State the blood parasite species.
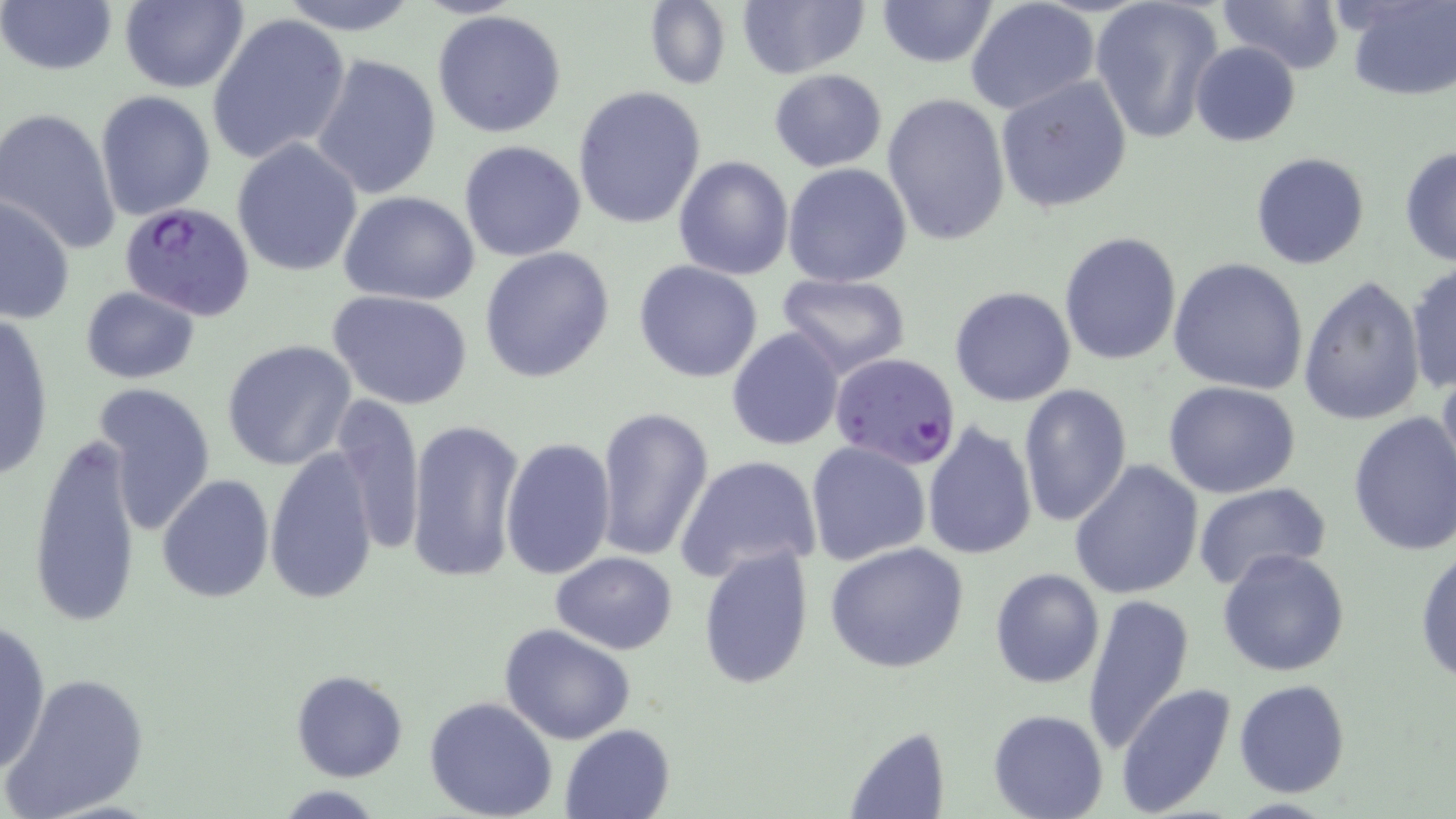

Plasmodium falciparum.

Approximate bounding boxes as named x1/y1/x2/y2 corners in pixels. Plasmodium falciparum-infected red blood cell locations: (x1=118, y1=199, x2=257, y2=323), (x1=830, y1=351, x2=961, y2=468). Uninfected red blood cell locations: (x1=118, y1=0, x2=249, y2=94), (x1=273, y1=0, x2=422, y2=34), (x1=735, y1=0, x2=869, y2=78), (x1=1089, y1=0, x2=1224, y2=144), (x1=1218, y1=0, x2=1346, y2=75), (x1=1341, y1=0, x2=1456, y2=100), (x1=2, y1=1, x2=119, y2=78), (x1=876, y1=1, x2=997, y2=70), (x1=642, y1=2, x2=732, y2=90), (x1=965, y1=2, x2=1099, y2=117), (x1=432, y1=9, x2=568, y2=137), (x1=208, y1=13, x2=352, y2=167), (x1=1190, y1=42, x2=1301, y2=147), (x1=311, y1=54, x2=443, y2=200), (x1=769, y1=69, x2=887, y2=172), (x1=995, y1=75, x2=1134, y2=212), (x1=571, y1=85, x2=707, y2=230), (x1=94, y1=89, x2=217, y2=223), (x1=882, y1=91, x2=1012, y2=248), (x1=0, y1=105, x2=122, y2=257), (x1=231, y1=139, x2=363, y2=276), (x1=459, y1=139, x2=586, y2=261), (x1=1398, y1=144, x2=1456, y2=268), (x1=1250, y1=151, x2=1370, y2=269), (x1=673, y1=156, x2=794, y2=280), (x1=783, y1=161, x2=914, y2=286), (x1=339, y1=190, x2=482, y2=307), (x1=1, y1=196, x2=75, y2=324), (x1=1060, y1=232, x2=1182, y2=365), (x1=478, y1=247, x2=616, y2=383), (x1=1169, y1=258, x2=1310, y2=395), (x1=633, y1=261, x2=764, y2=384), (x1=1405, y1=263, x2=1455, y2=396), (x1=775, y1=273, x2=912, y2=379), (x1=1298, y1=276, x2=1426, y2=427), (x1=79, y1=286, x2=200, y2=383), (x1=949, y1=287, x2=1077, y2=407), (x1=327, y1=289, x2=474, y2=410), (x1=1, y1=311, x2=56, y2=483), (x1=726, y1=327, x2=845, y2=451), (x1=221, y1=339, x2=357, y2=471), (x1=1434, y1=366, x2=1456, y2=500), (x1=95, y1=379, x2=217, y2=533), (x1=1163, y1=382, x2=1300, y2=499), (x1=1018, y1=383, x2=1134, y2=526), (x1=330, y1=393, x2=425, y2=559), (x1=593, y1=405, x2=714, y2=565), (x1=1348, y1=410, x2=1456, y2=558), (x1=405, y1=418, x2=524, y2=584), (x1=921, y1=421, x2=1035, y2=562), (x1=26, y1=431, x2=143, y2=629), (x1=502, y1=436, x2=617, y2=580), (x1=805, y1=442, x2=932, y2=566), (x1=264, y1=451, x2=380, y2=604), (x1=677, y1=456, x2=822, y2=581), (x1=1069, y1=459, x2=1204, y2=599), (x1=156, y1=473, x2=274, y2=603), (x1=1190, y1=482, x2=1333, y2=596), (x1=824, y1=541, x2=970, y2=673), (x1=1414, y1=542, x2=1456, y2=688), (x1=697, y1=545, x2=815, y2=688), (x1=1216, y1=549, x2=1351, y2=678), (x1=550, y1=552, x2=678, y2=654), (x1=989, y1=567, x2=1104, y2=689), (x1=1082, y1=593, x2=1195, y2=754), (x1=0, y1=620, x2=52, y2=777), (x1=499, y1=624, x2=637, y2=745), (x1=291, y1=669, x2=409, y2=783), (x1=5, y1=671, x2=152, y2=817), (x1=1234, y1=678, x2=1350, y2=798), (x1=1115, y1=682, x2=1238, y2=817), (x1=424, y1=695, x2=558, y2=819), (x1=988, y1=709, x2=1109, y2=819), (x1=559, y1=723, x2=676, y2=819), (x1=843, y1=728, x2=950, y2=818). Light microscopy. Single field of view. May-Grünwald-Giemsa stain. 1000x magnification. Thin blood film. Image is 1456×819 pixels.